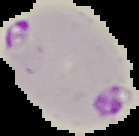

Cell region segmented out of the field of view; the surrounding area is masked to black. From a thin blood smear. Image is 139×136 pixels. Result: malaria parasites detected.